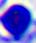
A leukocyte is shown. 400x magnification. Photomicrograph.